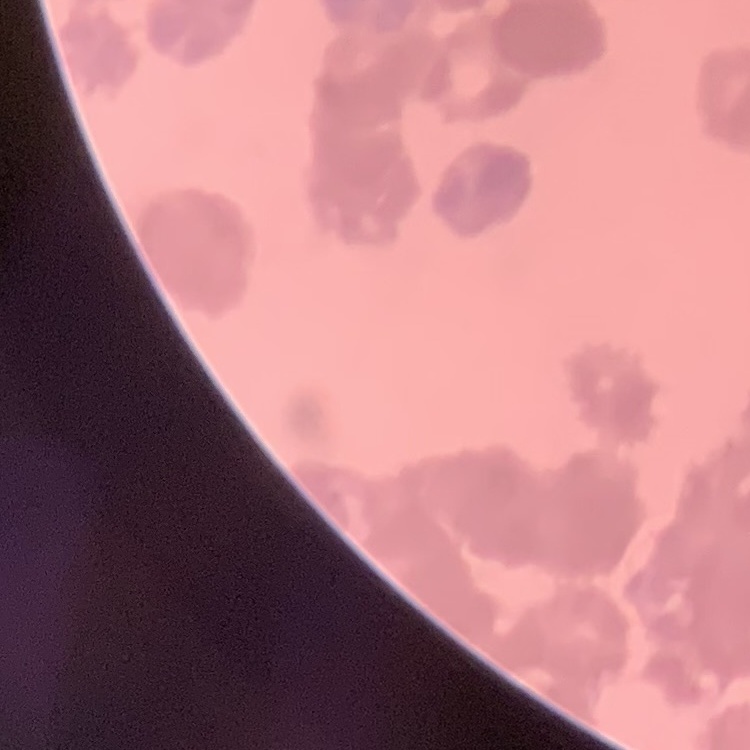

erythrocyte morphology = rouleaux formation
preparation = thin blood smear
image type = one tile cut from a larger photomicrograph
stain = Field's or Giemsa